Identify the preparation type.
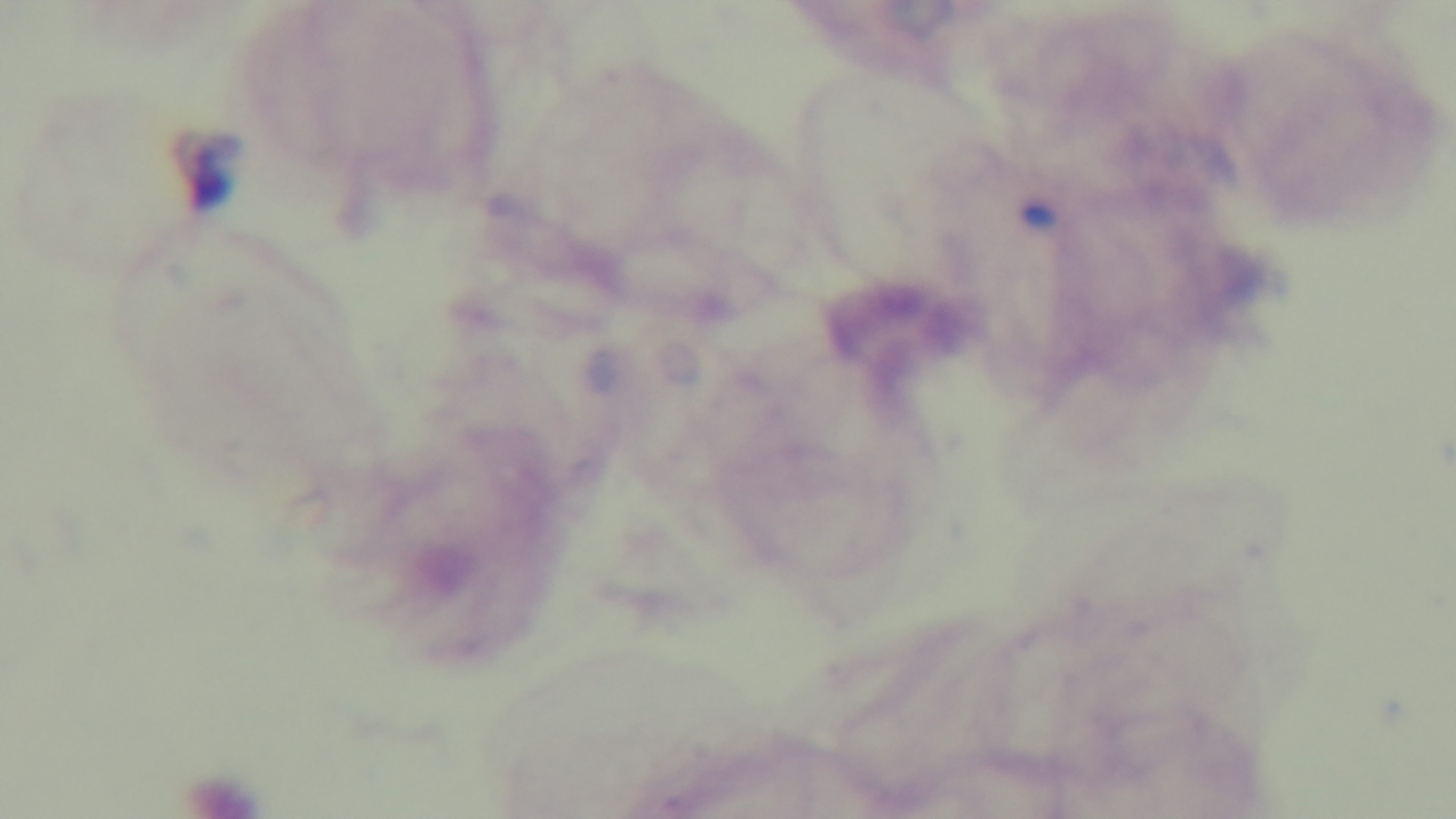
It is a thick blood film.

Malaria status: negative. Photomicrograph. One field from the slide. Mounted 4K digital camera. 100x oil-immersion objective. Giemsa stain.